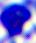
Summary:
  - Modality: photomicrograph
  - Magnification: 400x
  - Identification: white blood cell